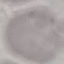
Result: no malaria parasites seen. Photographed with a smartphone camera at the microscope eyepiece. Giemsa stain. Cell patch, automatically extracted from a larger field of view and resized to 64 × 64 pixels. Thin smear of blood.